Classify this cell by malaria status.
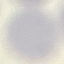
Uninfected.

Cell patch, automatically extracted from a larger field of view and resized to 64 × 64 pixels. Photographed with a smartphone camera at the microscope eyepiece. Thin blood smear. Giemsa-stained preparation.